Assess the morphology of the erythrocytes.
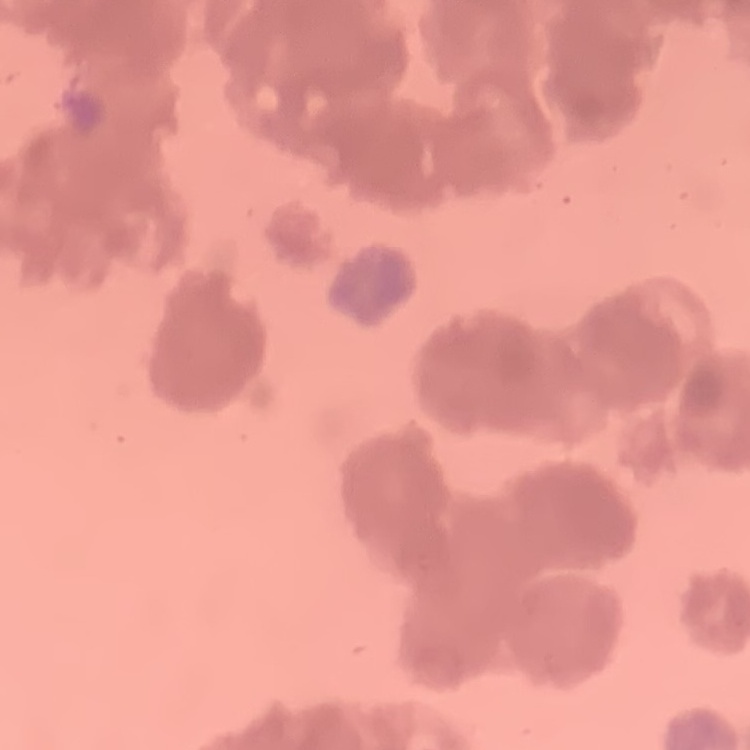
They show rouleaux formation.

Summary:
  - Stain: Field's or Giemsa
  - Preparation: thin peripheral smear
  - Image type: square crop of a larger photomicrograph